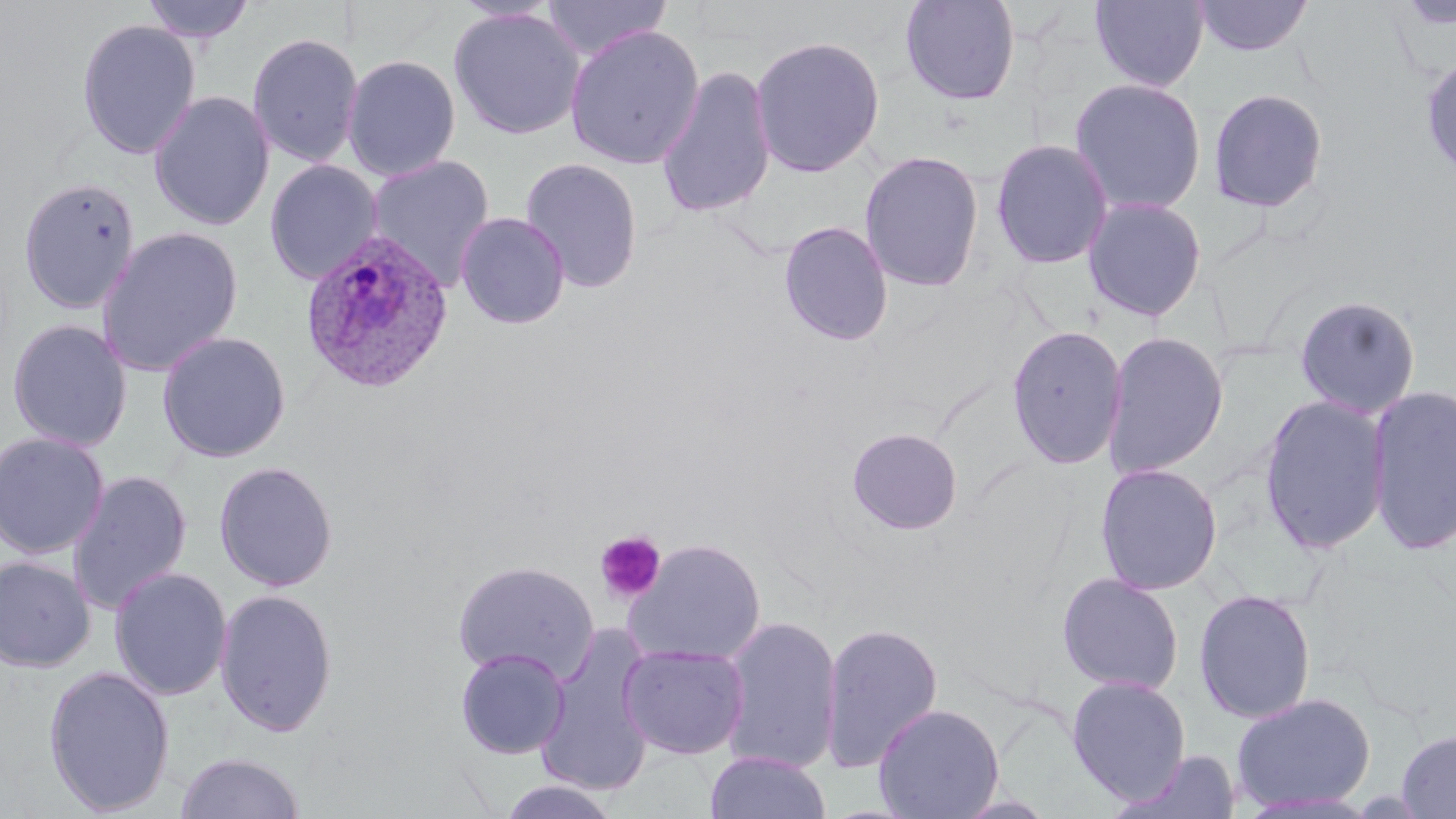
Summary:
  - Coordinate format: approximate bounding boxes as named x1/y1/x2/y2 corners in pixels
  - Uninfected red blood cell locations: (x1=139, y1=0, x2=256, y2=46), (x1=542, y1=0, x2=672, y2=61), (x1=899, y1=0, x2=1021, y2=106), (x1=1089, y1=0, x2=1210, y2=92), (x1=1193, y1=0, x2=1314, y2=58), (x1=1395, y1=0, x2=1456, y2=31), (x1=448, y1=7, x2=585, y2=140), (x1=76, y1=18, x2=201, y2=160), (x1=564, y1=24, x2=705, y2=169), (x1=247, y1=31, x2=364, y2=168), (x1=749, y1=34, x2=886, y2=178), (x1=1420, y1=53, x2=1456, y2=186), (x1=342, y1=54, x2=461, y2=182), (x1=656, y1=64, x2=777, y2=219), (x1=1068, y1=77, x2=1207, y2=216), (x1=1207, y1=87, x2=1329, y2=213), (x1=149, y1=90, x2=275, y2=231), (x1=990, y1=138, x2=1114, y2=270), (x1=859, y1=150, x2=985, y2=292), (x1=366, y1=154, x2=495, y2=291), (x1=519, y1=157, x2=644, y2=294), (x1=264, y1=159, x2=384, y2=286), (x1=18, y1=176, x2=141, y2=315), (x1=1082, y1=196, x2=1207, y2=322), (x1=455, y1=212, x2=570, y2=329), (x1=778, y1=220, x2=894, y2=347), (x1=95, y1=227, x2=244, y2=377), (x1=1293, y1=295, x2=1421, y2=420), (x1=6, y1=318, x2=133, y2=452), (x1=1006, y1=324, x2=1127, y2=470), (x1=156, y1=330, x2=292, y2=463), (x1=1102, y1=331, x2=1230, y2=480), (x1=1366, y1=385, x2=1456, y2=556), (x1=1258, y1=394, x2=1391, y2=556), (x1=846, y1=427, x2=964, y2=535), (x1=0, y1=431, x2=110, y2=560), (x1=213, y1=460, x2=339, y2=592), (x1=1094, y1=462, x2=1223, y2=596), (x1=67, y1=469, x2=193, y2=615), (x1=624, y1=538, x2=766, y2=667), (x1=0, y1=555, x2=96, y2=672), (x1=451, y1=560, x2=599, y2=684), (x1=109, y1=566, x2=232, y2=701), (x1=1056, y1=572, x2=1185, y2=696), (x1=214, y1=587, x2=339, y2=738), (x1=1193, y1=589, x2=1316, y2=724), (x1=718, y1=616, x2=844, y2=775), (x1=819, y1=621, x2=944, y2=775), (x1=536, y1=627, x2=658, y2=798), (x1=618, y1=643, x2=750, y2=759), (x1=454, y1=647, x2=570, y2=759), (x1=42, y1=665, x2=176, y2=816), (x1=1066, y1=676, x2=1191, y2=804), (x1=1230, y1=691, x2=1376, y2=813), (x1=873, y1=703, x2=1005, y2=819), (x1=1396, y1=729, x2=1456, y2=818), (x1=1109, y1=749, x2=1243, y2=819), (x1=704, y1=750, x2=830, y2=819), (x1=174, y1=751, x2=306, y2=819), (x1=496, y1=778, x2=620, y2=818)
  - Platelet locations: (x1=594, y1=531, x2=666, y2=604)
  - Plasmodium ovale-infected red blood cell locations: (x1=300, y1=230, x2=455, y2=395)
  - Slide-level diagnosis: Plasmodium ovale
  - Image size: 1456×819 pixels
  - Stain: May-Grünwald-Giemsa
  - Preparation: thin blood film
  - Magnification: 1000x
  - Modality: light microscopy
  - Field of view: single